Outline each blood parasite and name the species.
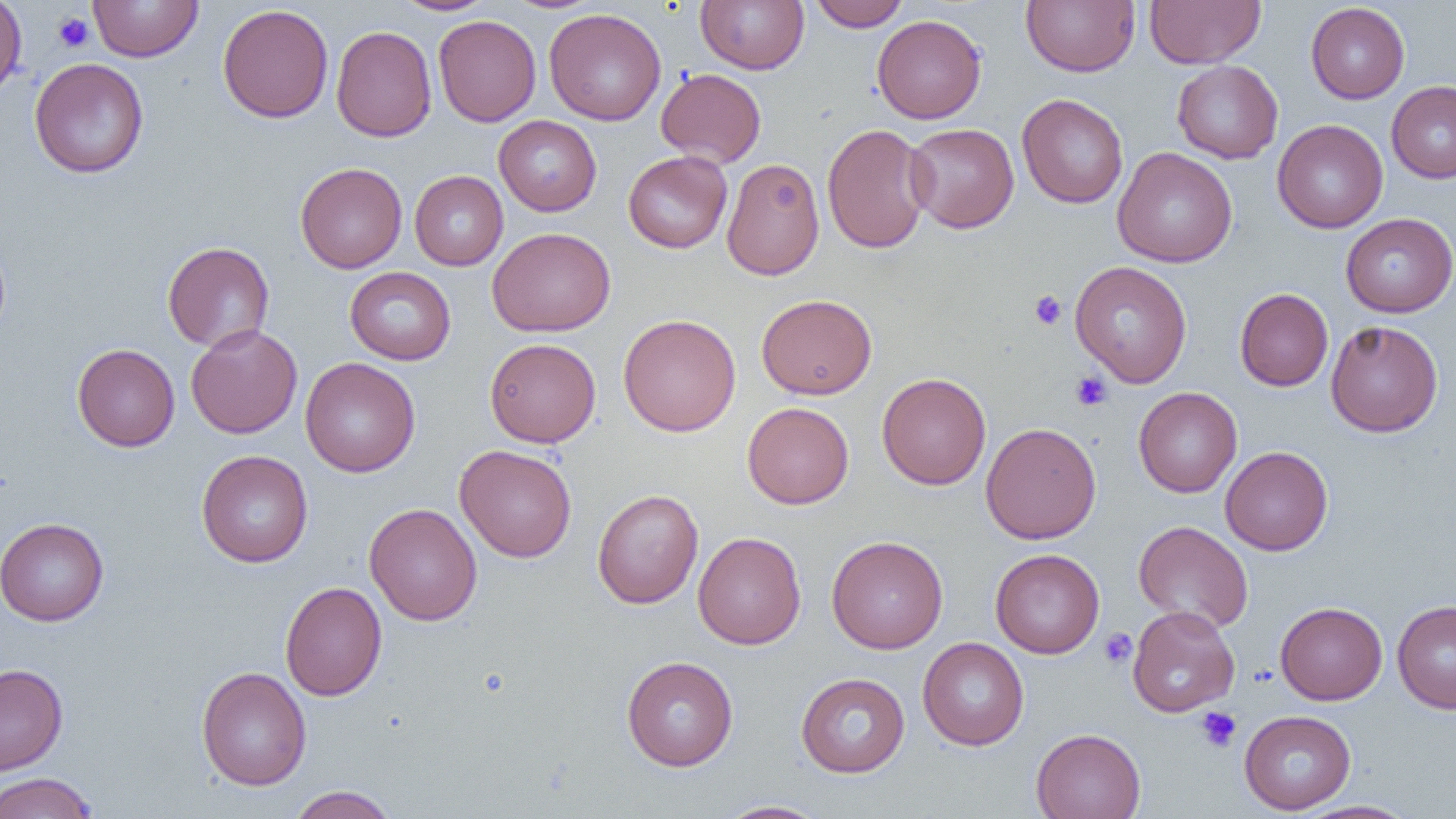
No blood parasites observed.

Approximate bounding boxes as named x1/y1/x2/y2 corners in pixels. Platelet locations: (x1=53, y1=12, x2=93, y2=52), (x1=1029, y1=290, x2=1067, y2=331), (x1=1070, y1=371, x2=1113, y2=411), (x1=1100, y1=629, x2=1138, y2=668), (x1=1196, y1=706, x2=1242, y2=752). Uninfected red blood cell locations: (x1=0, y1=0, x2=27, y2=98), (x1=88, y1=0, x2=203, y2=62), (x1=391, y1=0, x2=499, y2=16), (x1=695, y1=0, x2=809, y2=74), (x1=808, y1=0, x2=911, y2=30), (x1=1021, y1=0, x2=1140, y2=77), (x1=1144, y1=0, x2=1265, y2=68), (x1=1305, y1=2, x2=1410, y2=104), (x1=217, y1=4, x2=333, y2=123), (x1=543, y1=8, x2=666, y2=125), (x1=872, y1=14, x2=987, y2=124), (x1=433, y1=15, x2=541, y2=127), (x1=331, y1=25, x2=436, y2=142), (x1=29, y1=58, x2=149, y2=179), (x1=1172, y1=60, x2=1283, y2=163), (x1=656, y1=68, x2=767, y2=167), (x1=1386, y1=81, x2=1456, y2=183), (x1=1017, y1=93, x2=1128, y2=208), (x1=494, y1=115, x2=602, y2=216), (x1=1272, y1=119, x2=1388, y2=233), (x1=822, y1=123, x2=932, y2=254), (x1=904, y1=123, x2=1019, y2=233), (x1=1112, y1=147, x2=1237, y2=268), (x1=623, y1=150, x2=733, y2=253), (x1=721, y1=158, x2=825, y2=280), (x1=295, y1=162, x2=407, y2=273), (x1=410, y1=170, x2=508, y2=270), (x1=1340, y1=213, x2=1456, y2=317), (x1=487, y1=227, x2=616, y2=337), (x1=162, y1=241, x2=275, y2=352), (x1=1070, y1=261, x2=1192, y2=387), (x1=344, y1=266, x2=456, y2=365), (x1=1235, y1=288, x2=1333, y2=391), (x1=756, y1=294, x2=877, y2=399), (x1=618, y1=313, x2=741, y2=436), (x1=1325, y1=320, x2=1443, y2=437), (x1=186, y1=324, x2=303, y2=439), (x1=474, y1=338, x2=586, y2=561), (x1=484, y1=338, x2=601, y2=447), (x1=72, y1=343, x2=180, y2=452), (x1=300, y1=358, x2=420, y2=477), (x1=877, y1=372, x2=991, y2=490), (x1=1133, y1=387, x2=1242, y2=497), (x1=742, y1=402, x2=854, y2=509), (x1=980, y1=422, x2=1101, y2=544), (x1=454, y1=445, x2=577, y2=563), (x1=1220, y1=446, x2=1333, y2=555), (x1=196, y1=449, x2=313, y2=567), (x1=592, y1=488, x2=704, y2=608), (x1=364, y1=502, x2=482, y2=626), (x1=0, y1=517, x2=109, y2=626), (x1=1134, y1=520, x2=1254, y2=633), (x1=693, y1=531, x2=806, y2=650), (x1=826, y1=535, x2=948, y2=653), (x1=990, y1=548, x2=1105, y2=658), (x1=280, y1=581, x2=387, y2=701), (x1=1392, y1=600, x2=1456, y2=713), (x1=1274, y1=601, x2=1387, y2=705), (x1=1126, y1=605, x2=1239, y2=717), (x1=917, y1=637, x2=1029, y2=750), (x1=622, y1=655, x2=738, y2=771), (x1=0, y1=663, x2=68, y2=776), (x1=196, y1=666, x2=312, y2=790), (x1=796, y1=672, x2=910, y2=777), (x1=1239, y1=710, x2=1356, y2=814), (x1=1031, y1=728, x2=1146, y2=819), (x1=0, y1=772, x2=99, y2=818), (x1=288, y1=785, x2=398, y2=819), (x1=717, y1=800, x2=828, y2=819), (x1=1292, y1=800, x2=1419, y2=819). Slide-level diagnosis: no evidence of blood parasites. Thin blood smear. Captured at 1000x magnification. Image is 1456×819 pixels. Light microscopy. Single field of view.